Point out every malaria parasite and every leukocyte.
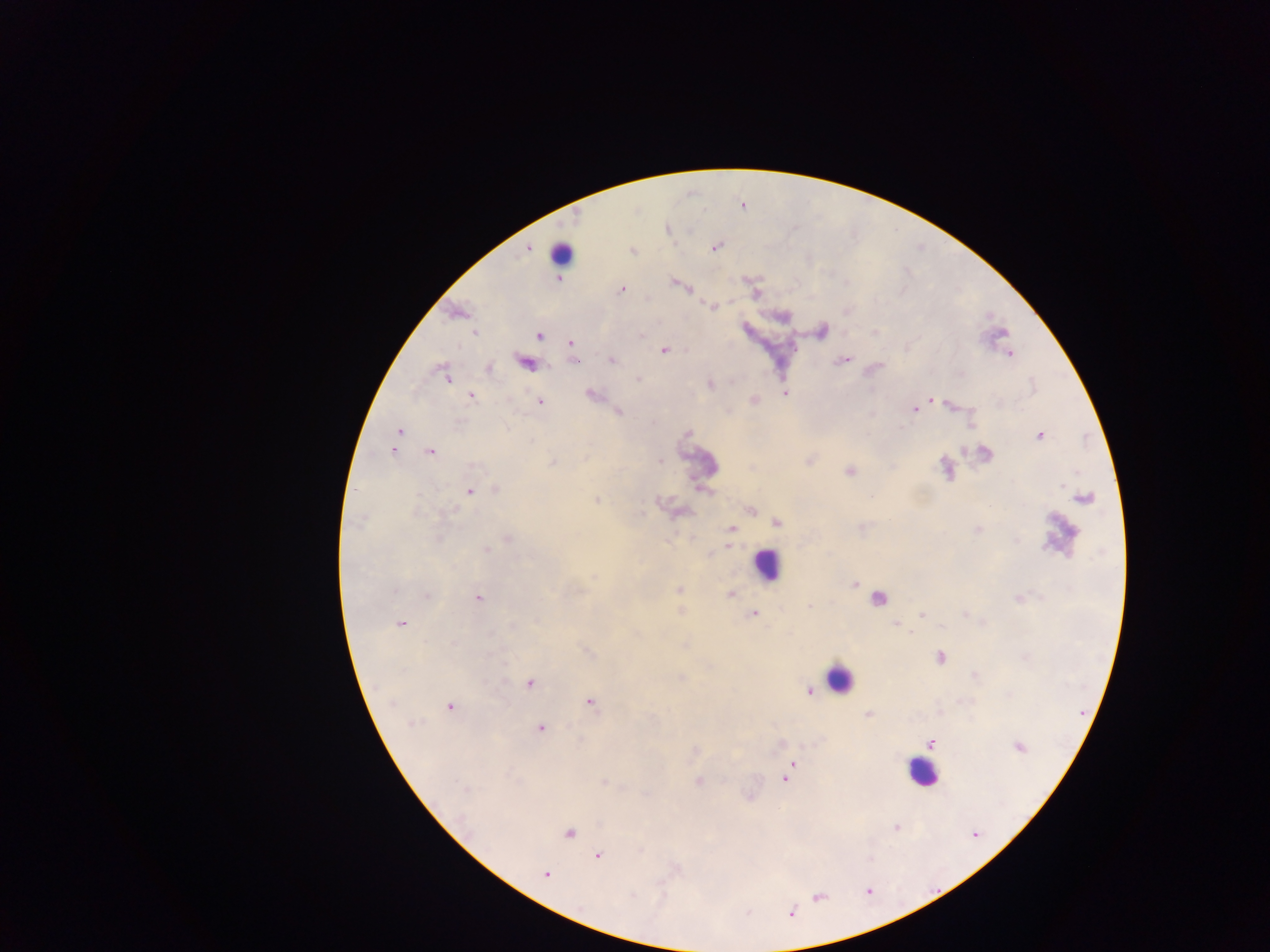
Approximate centers as {x, y} in pixels.
Malaria parasites: {714, 247}, {622, 289}, {475, 333}, {539, 336}, {570, 343}, {664, 350}, {489, 369}, {448, 379}, {472, 397}, {931, 400}, {540, 401}, {915, 410}, {398, 430}, {1039, 436}, {393, 450}, {429, 451}, {496, 489}, {469, 491}, {487, 550}, {427, 596}, {478, 597}, {754, 613}, {401, 624}, {453, 643}, {529, 684}, {589, 703}, {449, 706}, {869, 715}, {411, 723}, {541, 728}, {931, 743}, {789, 768}, {786, 776}, {699, 781}, {465, 791}, {569, 833}, {598, 856}, {546, 874}.
Leukocytes: {558, 256}, {765, 565}, {878, 600}, {839, 679}, {922, 772}.

{
  "country": "Ghana",
  "image_size": "1270×952 pixels",
  "field_of_view": "single",
  "preparation": "thick blood film",
  "capture": "mobile-phone photograph through a microscope"
}